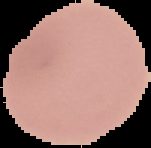
image size = 151×148 pixels
result = no malaria parasites detected
preparation = thin blood film
image type = cell region segmented out of the field of view; surrounding area masked to black